Assess this cell for malaria.
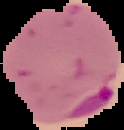
Parasitized.

Summary:
  - Preparation: thin blood film
  - Image type: cell region segmented out of the field of view; surrounding area masked to black
  - Image size: 124×130 pixels